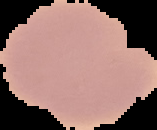
From a thin blood smear. Image is 157×130 pixels. Segmented cell region on a black background. Malaria status: uninfected.